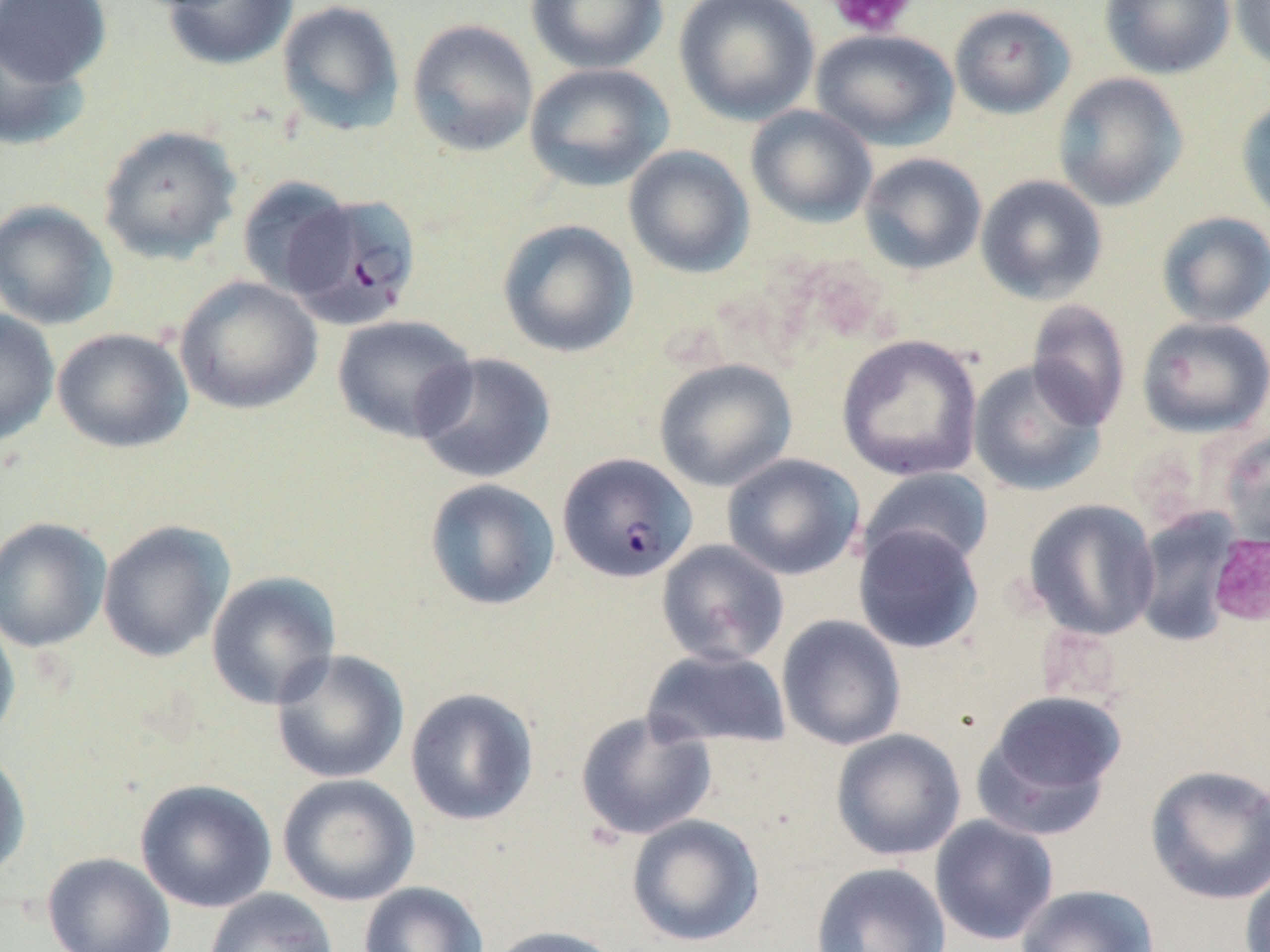
Approximate bounding boxes as (x1, y1, x2, y2) in pixels. Plasmodium falciparum-infected red blood cell locations: (286, 193, 421, 328), (557, 452, 697, 583). Platelet locations: (829, 0, 916, 38), (1207, 533, 1270, 627). Uninfected red blood cell locations: (1, 0, 112, 87), (161, 0, 298, 71), (277, 0, 405, 135), (525, 0, 668, 75), (674, 0, 820, 125), (1099, 0, 1236, 80), (1231, 0, 1270, 74), (949, 3, 1076, 120), (406, 18, 539, 157), (0, 23, 93, 152), (811, 28, 959, 151), (524, 63, 674, 192), (1052, 72, 1188, 212), (1235, 95, 1270, 229), (745, 105, 878, 228), (97, 124, 242, 265), (623, 145, 755, 278), (859, 152, 987, 275), (975, 174, 1108, 304), (237, 175, 355, 298), (0, 199, 117, 330), (1156, 211, 1270, 328), (497, 219, 639, 359), (174, 275, 323, 415), (1025, 300, 1131, 431), (0, 309, 60, 448), (332, 314, 477, 443), (1136, 315, 1270, 438), (52, 327, 193, 453), (836, 334, 983, 482), (412, 352, 556, 484), (653, 358, 797, 492), (967, 360, 1106, 496), (1217, 429, 1270, 547), (721, 453, 865, 581), (860, 467, 994, 572), (424, 478, 560, 611), (1022, 499, 1161, 641), (1132, 509, 1241, 647), (0, 516, 112, 653), (97, 520, 235, 663), (853, 524, 985, 654), (656, 539, 790, 667), (206, 571, 341, 710), (0, 610, 21, 744), (776, 615, 906, 751), (641, 648, 792, 751), (271, 649, 410, 785), (405, 687, 540, 826), (973, 690, 1127, 838), (574, 710, 717, 841), (830, 728, 966, 861), (0, 748, 31, 884), (1144, 763, 1269, 905), (277, 773, 420, 907), (134, 779, 277, 913), (626, 814, 765, 947), (930, 815, 1059, 946), (42, 851, 176, 952), (810, 862, 951, 952), (1240, 864, 1270, 952), (358, 881, 489, 952), (1014, 883, 1160, 952), (204, 888, 338, 952), (488, 924, 624, 952). Slide-level diagnosis: Plasmodium falciparum. 1000x magnification. Image is 1270×952 pixels. Thin blood film. May-Grünwald-Giemsa-stained preparation. One field of a larger specimen. Optical microscopy.